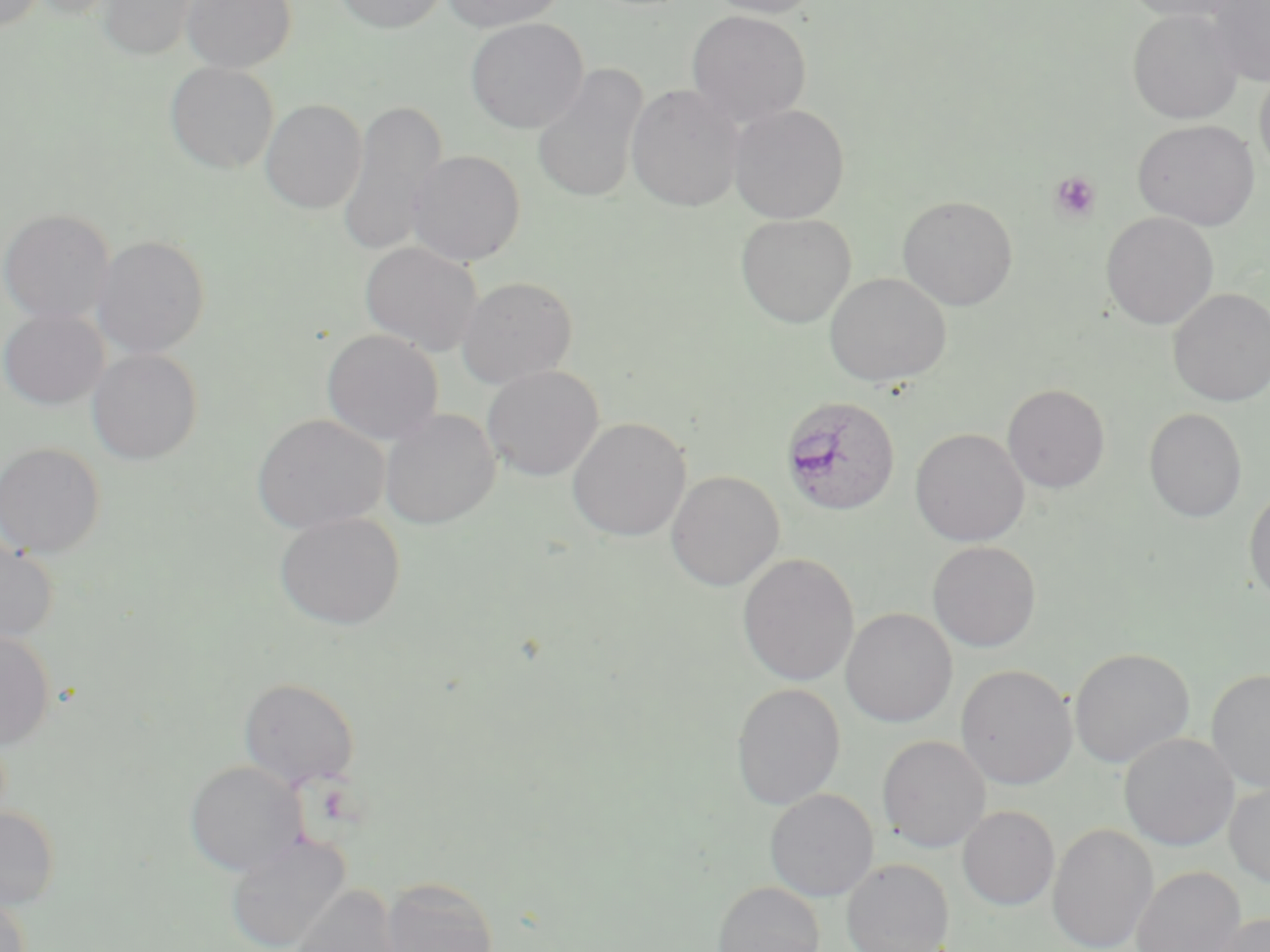
Summary:
  - Coordinate format: approximate bounding boxes as named x1/y1/x2/y2 corners in pixels
  - Uninfected red blood cell locations: (x1=0, y1=0, x2=46, y2=32), (x1=26, y1=0, x2=122, y2=20), (x1=96, y1=0, x2=200, y2=61), (x1=181, y1=0, x2=297, y2=73), (x1=332, y1=0, x2=449, y2=33), (x1=441, y1=0, x2=568, y2=32), (x1=704, y1=0, x2=821, y2=18), (x1=1119, y1=0, x2=1244, y2=22), (x1=1207, y1=0, x2=1270, y2=85), (x1=1127, y1=8, x2=1244, y2=124), (x1=685, y1=9, x2=812, y2=127), (x1=465, y1=18, x2=589, y2=134), (x1=165, y1=61, x2=279, y2=174), (x1=531, y1=63, x2=649, y2=204), (x1=1254, y1=66, x2=1270, y2=180), (x1=626, y1=84, x2=743, y2=211), (x1=260, y1=99, x2=367, y2=214), (x1=338, y1=99, x2=447, y2=259), (x1=728, y1=104, x2=850, y2=223), (x1=1133, y1=119, x2=1260, y2=230), (x1=407, y1=150, x2=526, y2=266), (x1=897, y1=195, x2=1018, y2=310), (x1=0, y1=208, x2=115, y2=325), (x1=1102, y1=213, x2=1218, y2=330), (x1=736, y1=214, x2=856, y2=328), (x1=92, y1=235, x2=210, y2=359), (x1=360, y1=241, x2=483, y2=355), (x1=824, y1=272, x2=951, y2=388), (x1=457, y1=276, x2=578, y2=387), (x1=1168, y1=288, x2=1270, y2=406), (x1=0, y1=308, x2=109, y2=410), (x1=321, y1=329, x2=443, y2=445), (x1=87, y1=348, x2=203, y2=465), (x1=482, y1=365, x2=603, y2=481), (x1=1003, y1=384, x2=1110, y2=493), (x1=1144, y1=408, x2=1247, y2=522), (x1=380, y1=409, x2=500, y2=529), (x1=252, y1=414, x2=389, y2=533), (x1=568, y1=417, x2=691, y2=542), (x1=910, y1=428, x2=1029, y2=546), (x1=0, y1=442, x2=105, y2=559), (x1=666, y1=471, x2=785, y2=591), (x1=1244, y1=484, x2=1270, y2=606), (x1=274, y1=511, x2=406, y2=630), (x1=0, y1=534, x2=59, y2=645), (x1=927, y1=541, x2=1042, y2=652), (x1=738, y1=553, x2=859, y2=687), (x1=841, y1=608, x2=958, y2=727), (x1=0, y1=630, x2=55, y2=750), (x1=1069, y1=647, x2=1195, y2=769), (x1=956, y1=664, x2=1077, y2=789), (x1=1206, y1=668, x2=1270, y2=791), (x1=239, y1=677, x2=360, y2=790), (x1=731, y1=683, x2=845, y2=810), (x1=1119, y1=732, x2=1237, y2=851), (x1=877, y1=735, x2=990, y2=853), (x1=185, y1=761, x2=305, y2=876), (x1=1224, y1=780, x2=1270, y2=887), (x1=764, y1=788, x2=879, y2=901), (x1=957, y1=805, x2=1060, y2=911), (x1=0, y1=806, x2=60, y2=909), (x1=1047, y1=823, x2=1158, y2=952), (x1=225, y1=834, x2=351, y2=952), (x1=842, y1=858, x2=953, y2=952), (x1=1131, y1=866, x2=1246, y2=952), (x1=381, y1=876, x2=498, y2=952), (x1=713, y1=881, x2=825, y2=952), (x1=287, y1=884, x2=403, y2=952), (x1=0, y1=893, x2=31, y2=952), (x1=1207, y1=912, x2=1270, y2=952)
  - Plasmodium ovale-infected red blood cell locations: (x1=780, y1=396, x2=901, y2=516)
  - Platelet locations: (x1=1048, y1=171, x2=1101, y2=223)
  - Slide-level diagnosis: Plasmodium ovale
  - Field of view: one of a larger specimen
  - Preparation: thin blood film
  - Modality: optical microscopy
  - Image size: 1270×952 pixels
  - Stain: May-Grünwald-Giemsa
  - Magnification: 1000x